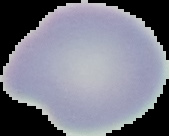

Result: no malaria parasites seen. From a thin blood film. Image is 169×136 pixels. The area outside the segmented cell region is set to black.